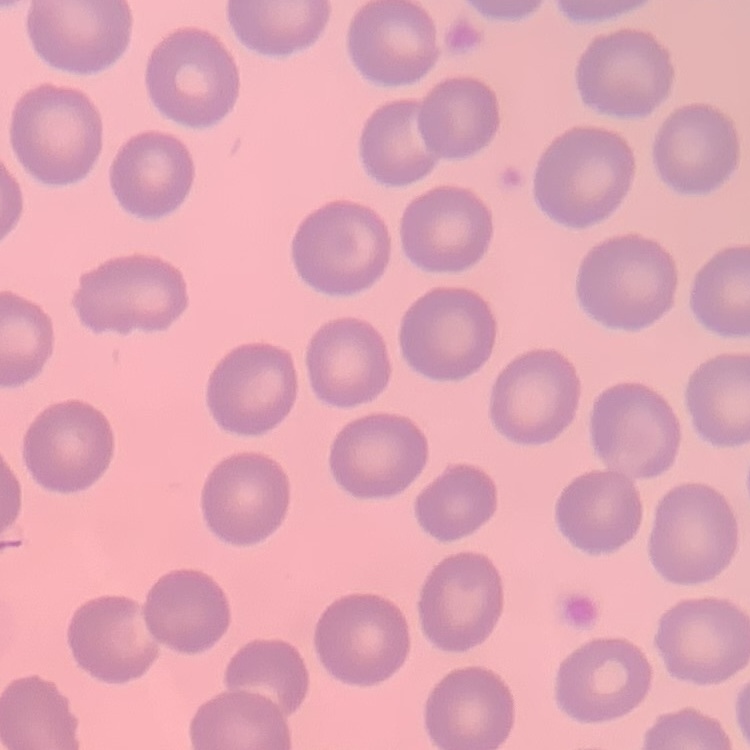

Summary:
  - Red blood cell morphology: no rouleaux formation
  - Preparation: thin blood smear
  - Stain: Field's or Giemsa
  - Image type: square crop of a larger photomicrograph